Name the parasite shown.
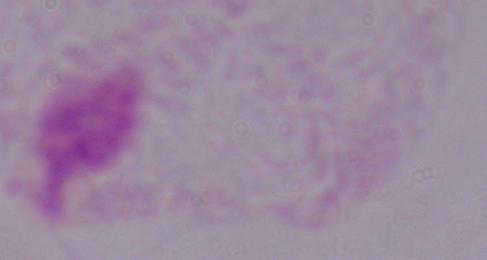

A trichomonad.

Summary:
  - Modality: micrograph
  - Magnification: 1000x